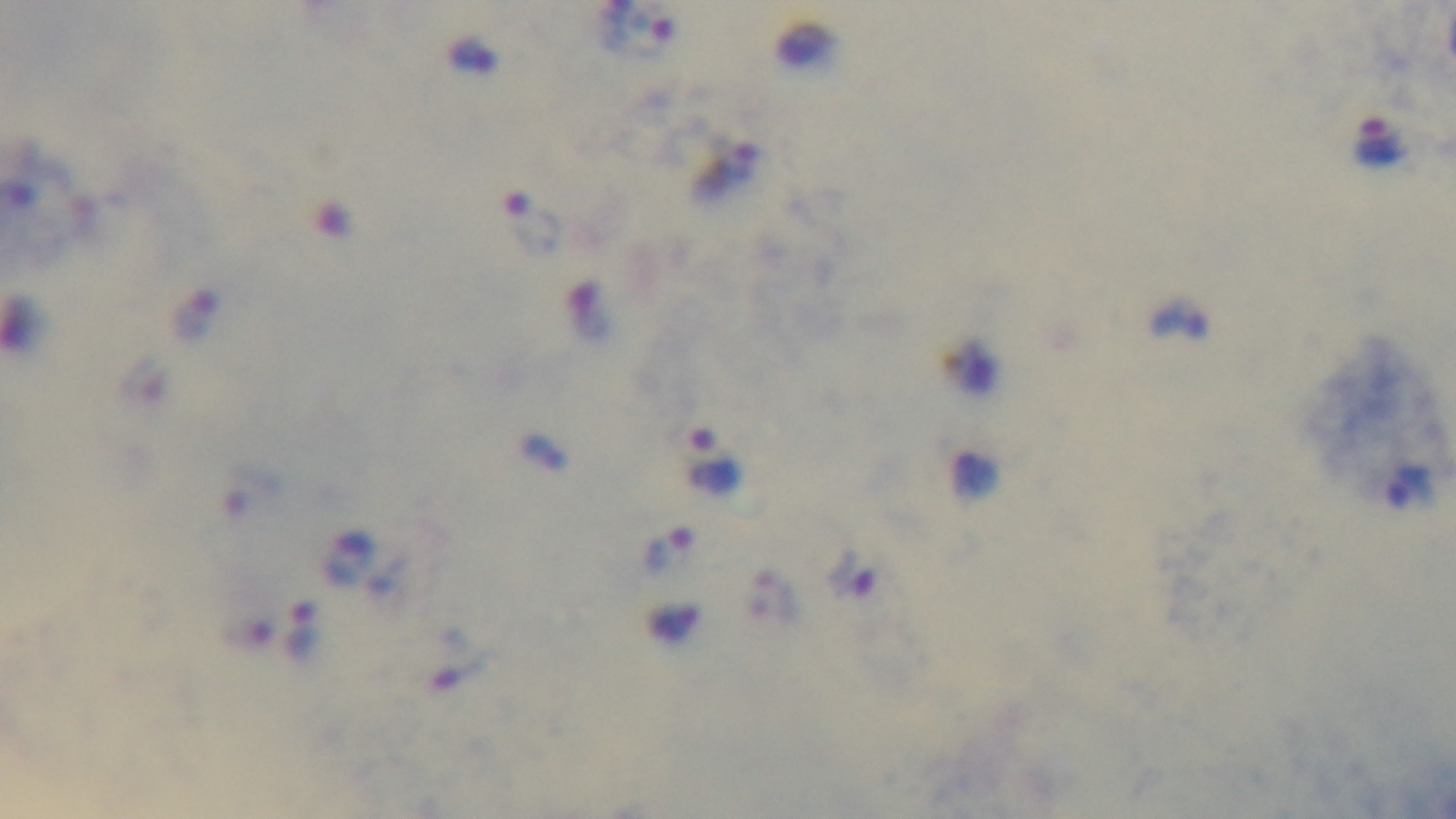
Summary:
  - Malaria status: infected
  - Objective: 100x oil immersion
  - Preparation: thick blood film
  - Capture: mounted 4K digital camera
  - Modality: light microscopy
  - Field of view: one from the slide
  - Stain: Giemsa